Locate every Plasmodium parasite.
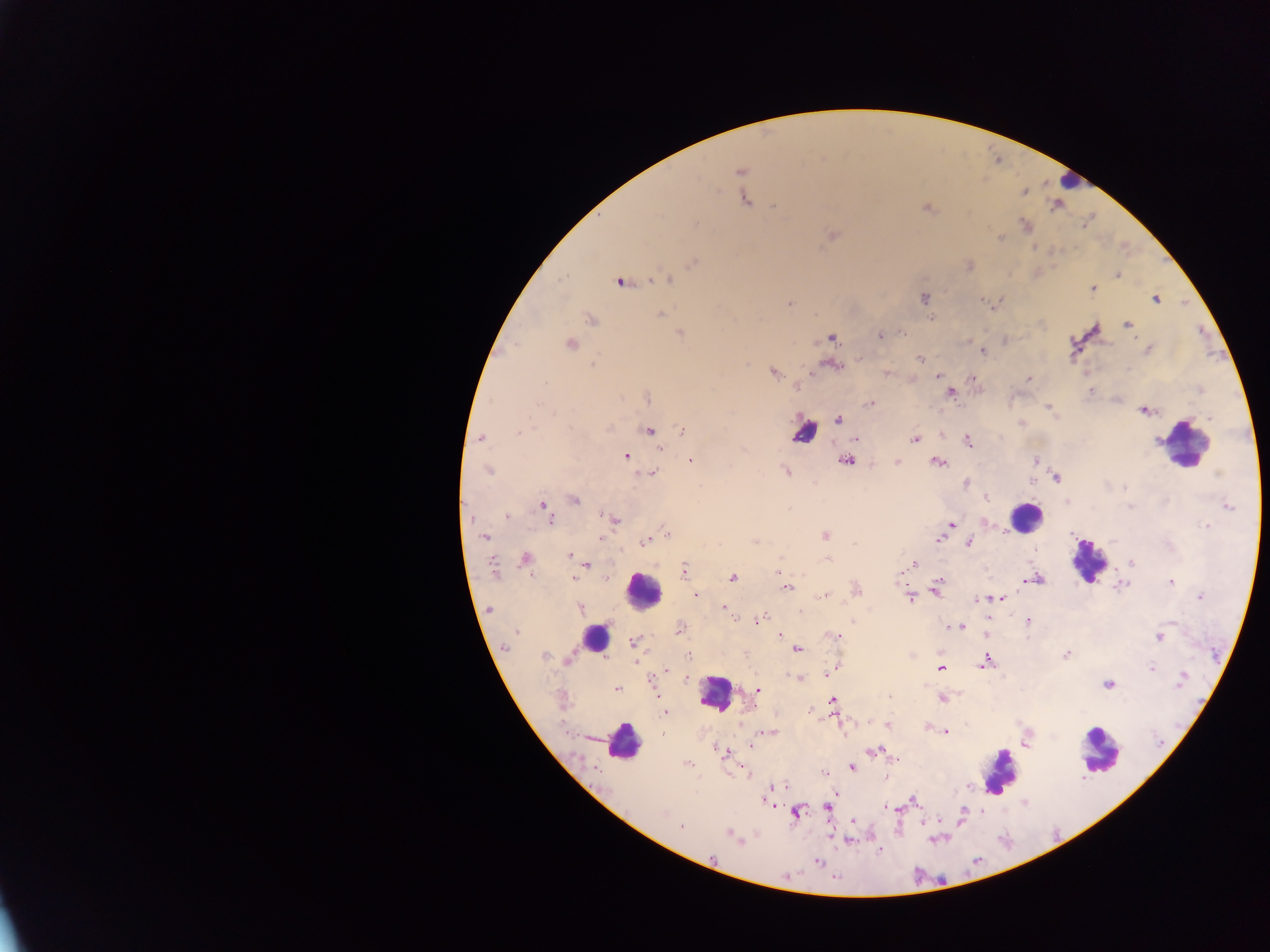

Approximate centers as x y in pixels.
Plasmodium parasites: 741 172; 1025 192; 744 200; 774 206; 926 209; 1025 225; 833 235; 999 238; 693 262; 1117 275; 667 279; 620 283; 1093 289; 925 297; 1155 299; 982 301; 789 303; 661 314; 931 318; 591 320; 1127 325; 902 332; 680 334; 881 335; 832 338; 570 343; 1148 349; 983 351; 860 358; 920 359; 593 364; 833 366; 886 372; 773 373; 938 375; 1029 378; 972 379; 798 387; 1090 390; 950 393; 647 397; 870 403; 538 404; 1049 407; 1144 410; 1210 418; 838 420; 607 429; 649 430; 683 431; 518 433; 481 438; 856 438; 915 438; 968 441; 659 448; 626 456; 691 460; 1035 460; 845 462; 897 462; 937 462; 488 471; 786 471; 653 474; 1217 475; 1056 478; 1030 481; 966 483; 1123 488; 986 497; 574 500; 544 506; 1130 507; 1229 507; 507 516; 549 519; 614 519; 950 524; 1207 526; 665 532; 826 536; 485 537; 600 539; 939 539; 646 541; 755 541; 969 543; 854 544; 569 556; 781 557; 526 559; 827 560; 1132 563; 587 564; 914 564; 493 567; 683 571; 900 573; 573 578; 732 578; 606 579; 1027 580; 1034 580; 1171 582; 1122 585; 938 586; 787 587; 857 590; 936 591; 824 595; 696 596; 910 597; 1200 597; 995 598; 1000 598; 982 599; 724 607; 580 609; 489 610; 800 610; 758 621; 1028 621; 955 626; 962 627; 680 629; 517 632; 986 634; 781 635; 836 636; 1159 637; 633 642; 506 646; 797 650; 1066 654; 544 656; 688 656; 569 659; 985 662; 941 668; 1152 668; 666 670; 833 670; 797 678; 652 680; 1181 680; 1109 685; 617 689; 757 690; 889 697; 942 699; 833 701; 665 712; 888 726; 946 731; 768 732; 663 735; 1027 743; 750 746; 720 751; 873 752; 893 758; 687 763; 852 767; 824 772; 781 787; 766 800; 913 801; 827 807; 888 807; 663 813; 795 813; 963 814; 852 822; 681 827; 730 834; 849 840; 879 850; 818 862.

preparation = thick blood smear
capture = mobile-phone photograph through a microscope
field of view = single
image size = 1270×952 pixels
country = Ghana
leukocyte locations = approximate centers as x y in pixels: 1069 182; 803 431; 1191 447; 1026 517; 1088 561; 643 590; 596 636; 716 693; 623 743; 1100 751; 999 771